Assess this cell for malaria.
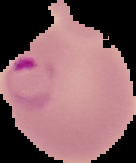
It is parasitized.

Summary:
  - Image size: 136×163 pixels
  - Preparation: thin blood smear
  - Image type: cell region segmented out of the field of view; surrounding area masked to black